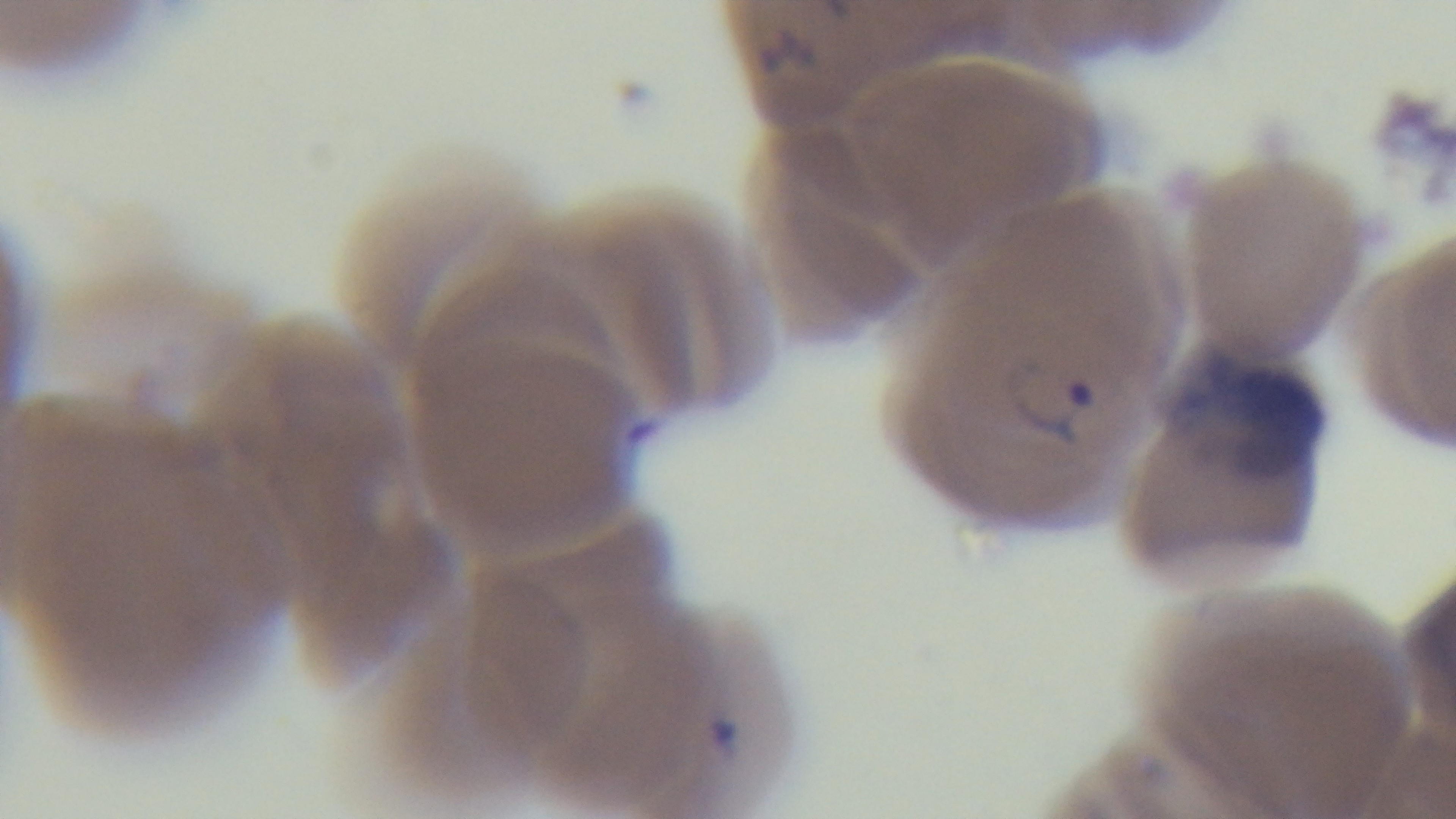
Summary:
  - Preparation: thin
  - Stain: Giemsa
  - Malaria status: infected
  - Field of view: one from the slide
  - Objective: 100x oil immersion
  - Modality: light microscopy
  - Capture: mounted 4K digital camera